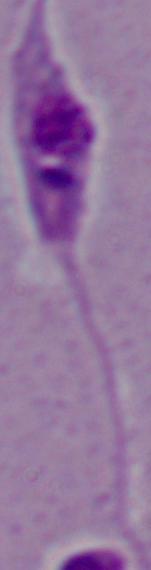

A Leishmania parasite is seen. Photomicrograph. Captured at 1000x magnification.